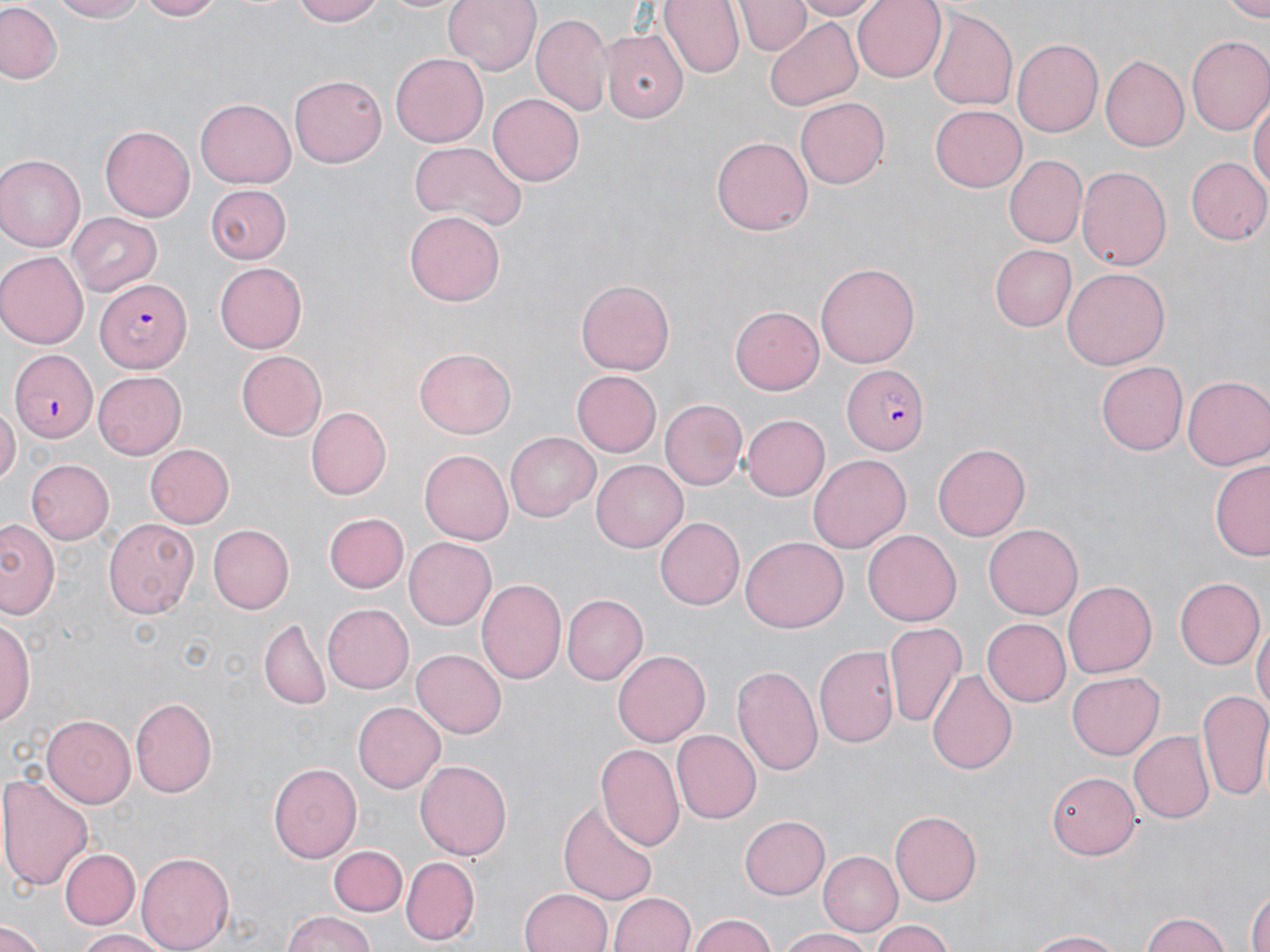
slide-level diagnosis = Plasmodium falciparum
image size = 1270×952 pixels
stain = May-Grünwald-Giemsa
magnification = 1000x
uninfected red blood cell locations = approximate bounding boxes as named x1/y1/x2/y2 corners in pixels: (x1=51, y1=0, x2=153, y2=23), (x1=135, y1=0, x2=227, y2=21), (x1=292, y1=0, x2=389, y2=25), (x1=376, y1=0, x2=470, y2=15), (x1=443, y1=0, x2=542, y2=75), (x1=659, y1=0, x2=745, y2=77), (x1=737, y1=0, x2=808, y2=55), (x1=795, y1=0, x2=877, y2=19), (x1=852, y1=0, x2=944, y2=81), (x1=1221, y1=1, x2=1270, y2=20), (x1=0, y1=3, x2=64, y2=84), (x1=928, y1=7, x2=1018, y2=114), (x1=532, y1=14, x2=612, y2=117), (x1=765, y1=18, x2=864, y2=110), (x1=602, y1=27, x2=687, y2=121), (x1=1186, y1=38, x2=1270, y2=137), (x1=1010, y1=39, x2=1102, y2=139), (x1=1102, y1=53, x2=1192, y2=151), (x1=391, y1=54, x2=488, y2=147), (x1=290, y1=74, x2=387, y2=167), (x1=487, y1=93, x2=583, y2=186), (x1=1251, y1=95, x2=1269, y2=198), (x1=197, y1=96, x2=295, y2=186), (x1=796, y1=97, x2=891, y2=188), (x1=930, y1=106, x2=1026, y2=191), (x1=101, y1=125, x2=194, y2=222), (x1=712, y1=136, x2=813, y2=235), (x1=409, y1=140, x2=526, y2=232), (x1=0, y1=154, x2=84, y2=252), (x1=1003, y1=155, x2=1087, y2=248), (x1=1185, y1=155, x2=1270, y2=245), (x1=1075, y1=167, x2=1170, y2=272), (x1=204, y1=185, x2=290, y2=265), (x1=405, y1=212, x2=505, y2=308), (x1=68, y1=213, x2=164, y2=297), (x1=991, y1=245, x2=1077, y2=330), (x1=0, y1=252, x2=86, y2=348), (x1=214, y1=262, x2=306, y2=353), (x1=816, y1=262, x2=918, y2=370), (x1=1062, y1=267, x2=1170, y2=370), (x1=577, y1=280, x2=675, y2=373), (x1=731, y1=306, x2=824, y2=394), (x1=415, y1=348, x2=516, y2=437), (x1=235, y1=351, x2=326, y2=440), (x1=1097, y1=362, x2=1189, y2=455), (x1=93, y1=372, x2=185, y2=459), (x1=573, y1=372, x2=660, y2=456), (x1=1182, y1=375, x2=1270, y2=471), (x1=661, y1=399, x2=747, y2=490), (x1=0, y1=405, x2=18, y2=486), (x1=307, y1=406, x2=393, y2=499), (x1=741, y1=413, x2=829, y2=499), (x1=507, y1=432, x2=599, y2=521), (x1=142, y1=443, x2=234, y2=529), (x1=933, y1=444, x2=1031, y2=540), (x1=421, y1=450, x2=512, y2=543), (x1=808, y1=454, x2=911, y2=552), (x1=24, y1=459, x2=113, y2=544), (x1=593, y1=460, x2=687, y2=552), (x1=1211, y1=461, x2=1270, y2=561), (x1=324, y1=512, x2=409, y2=593), (x1=1, y1=516, x2=61, y2=621), (x1=657, y1=516, x2=747, y2=610), (x1=104, y1=518, x2=199, y2=619), (x1=207, y1=524, x2=294, y2=614), (x1=984, y1=525, x2=1083, y2=619), (x1=864, y1=530, x2=961, y2=624), (x1=740, y1=536, x2=849, y2=633), (x1=404, y1=537, x2=497, y2=630), (x1=1174, y1=577, x2=1263, y2=669), (x1=476, y1=579, x2=565, y2=685), (x1=1062, y1=582, x2=1157, y2=679), (x1=563, y1=595, x2=646, y2=683), (x1=323, y1=603, x2=414, y2=693), (x1=1, y1=615, x2=36, y2=726), (x1=980, y1=618, x2=1070, y2=707), (x1=258, y1=620, x2=331, y2=709), (x1=886, y1=622, x2=966, y2=731), (x1=1253, y1=623, x2=1269, y2=718), (x1=815, y1=644, x2=898, y2=747), (x1=612, y1=647, x2=709, y2=743), (x1=411, y1=648, x2=507, y2=737), (x1=733, y1=665, x2=824, y2=777), (x1=928, y1=668, x2=1017, y2=777), (x1=1067, y1=672, x2=1165, y2=760), (x1=1197, y1=689, x2=1270, y2=801), (x1=130, y1=697, x2=218, y2=798), (x1=353, y1=701, x2=446, y2=793), (x1=42, y1=714, x2=134, y2=809), (x1=673, y1=730, x2=761, y2=823), (x1=1128, y1=731, x2=1213, y2=823), (x1=596, y1=741, x2=686, y2=852), (x1=414, y1=759, x2=513, y2=862), (x1=268, y1=763, x2=362, y2=864), (x1=1046, y1=769, x2=1138, y2=860), (x1=0, y1=773, x2=93, y2=890), (x1=559, y1=795, x2=658, y2=907), (x1=890, y1=812, x2=982, y2=904), (x1=740, y1=814, x2=831, y2=900), (x1=330, y1=846, x2=406, y2=916), (x1=59, y1=848, x2=140, y2=930), (x1=137, y1=850, x2=233, y2=952), (x1=819, y1=851, x2=901, y2=936), (x1=401, y1=856, x2=478, y2=945), (x1=1247, y1=881, x2=1269, y2=952), (x1=518, y1=889, x2=612, y2=952), (x1=610, y1=891, x2=695, y2=952), (x1=1137, y1=910, x2=1231, y2=952), (x1=279, y1=911, x2=380, y2=952), (x1=688, y1=914, x2=781, y2=952), (x1=0, y1=917, x2=44, y2=949), (x1=870, y1=919, x2=957, y2=952), (x1=780, y1=928, x2=878, y2=952), (x1=1022, y1=929, x2=1130, y2=950), (x1=70, y1=930, x2=174, y2=951)
preparation = thin blood smear
field of view = single
modality = light microscopy
Plasmodium falciparum-infected red blood cell locations = approximate bounding boxes as named x1/y1/x2/y2 corners in pixels: (x1=96, y1=277, x2=194, y2=370), (x1=9, y1=347, x2=98, y2=440), (x1=843, y1=365, x2=928, y2=453)